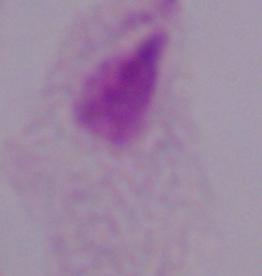
identification = trichomonad
modality = photomicrograph
magnification = 1000x